Report the malaria status of this cell.
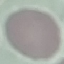
It is uninfected.

{
  "stain": "Giemsa",
  "capture": "smartphone camera at the microscope eyepiece",
  "image_type": "automatically extracted cell patch, resized to 64 × 64 pixels",
  "preparation": "thin blood smear"
}